Classify this cell by malaria status.
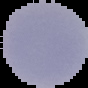
Uninfected.

preparation = thin blood film
image size = 88×88 pixels
image type = cell region segmented out of the field of view; surrounding area masked to black